State which cell type is depicted.
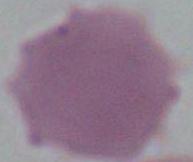
An erythrocyte.

modality = micrograph
magnification = 1000x